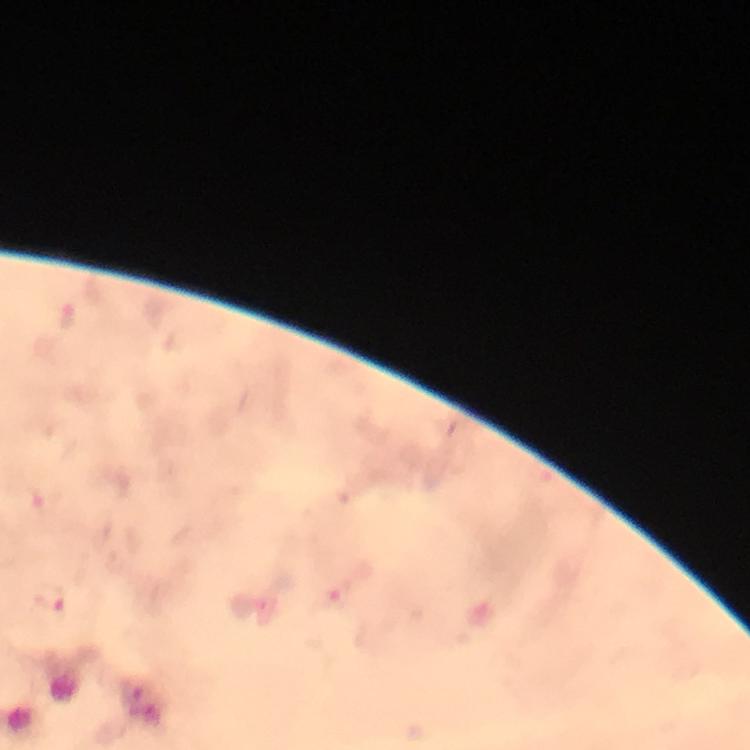
Plasmodium parasite locations = approximate centers as {x, y} in pixels: {68, 316}, {337, 594}, {52, 597}
image size = 750×750 pixels
preparation = thick blood film
context = from a diagnostic examination for malaria
cropped from = one field of view
immersion oil = used
capture = smartphone mounted on the microscope
magnification = 100x
stain = Giemsa